Identify the blood parasite species.
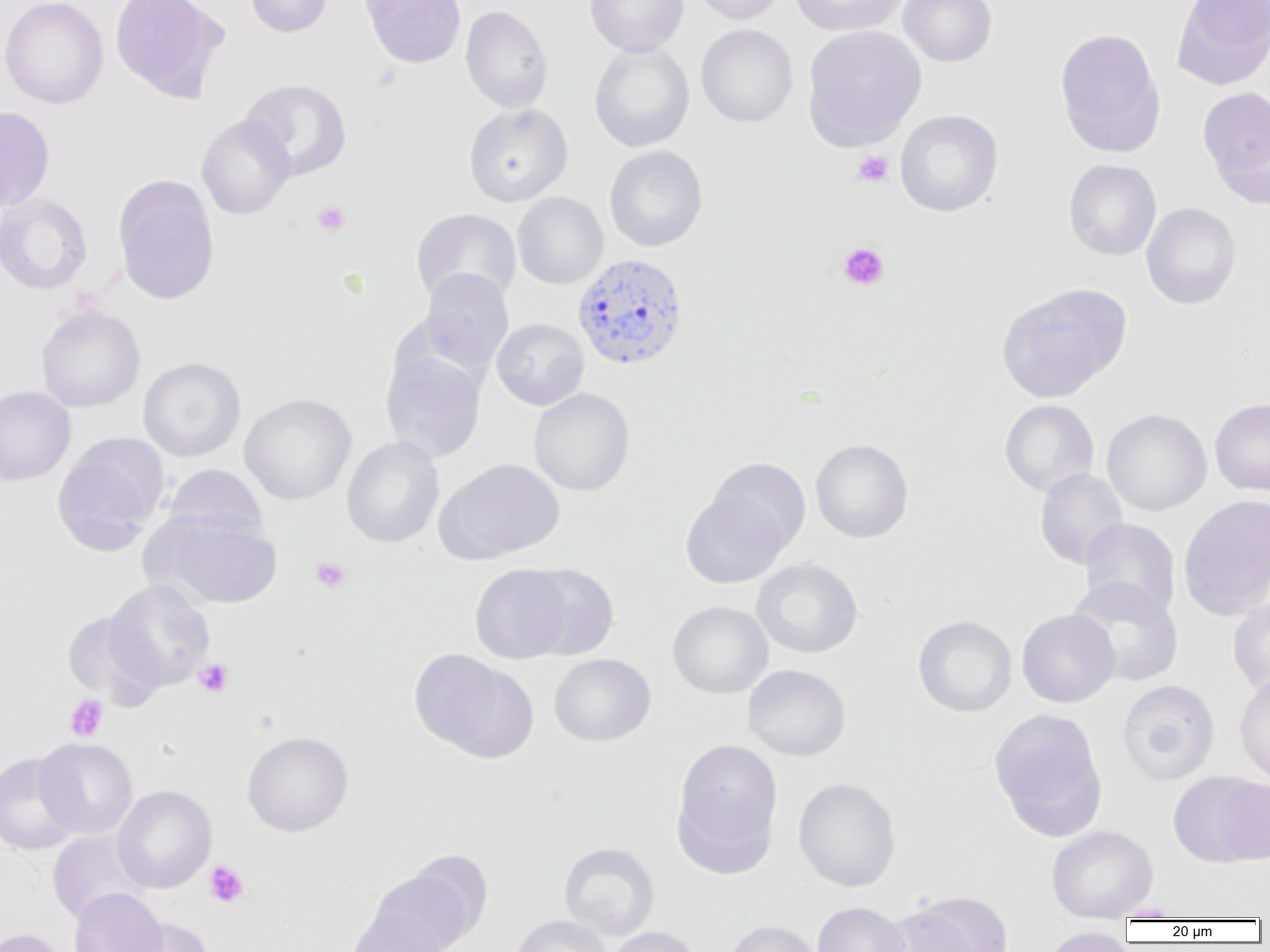

Plasmodium vivax.

uninfected red blood cell locations = approximate bounding boxes as (x1, y1, x2, y2) in pixels: (0, 0, 109, 108), (109, 0, 227, 101), (244, 0, 333, 37), (360, 0, 466, 68), (584, 0, 689, 57), (692, 0, 788, 25), (789, 0, 907, 36), (898, 0, 997, 67), (1173, 0, 1270, 90), (460, 4, 553, 113), (696, 24, 798, 127), (802, 25, 927, 150), (1055, 28, 1165, 158), (589, 42, 694, 151), (240, 78, 352, 181), (1198, 87, 1269, 202), (464, 103, 572, 206), (0, 106, 55, 212), (895, 109, 1003, 216), (196, 114, 296, 220), (605, 145, 707, 252), (1063, 159, 1161, 261), (113, 175, 220, 305), (512, 192, 608, 289), (0, 193, 92, 294), (1141, 202, 1241, 309), (411, 208, 521, 307), (417, 268, 513, 376), (996, 282, 1129, 403), (36, 305, 145, 412), (491, 318, 589, 410), (381, 351, 486, 462), (138, 356, 246, 462), (0, 386, 76, 485), (529, 387, 634, 495), (239, 393, 357, 505), (1210, 398, 1270, 496), (999, 399, 1099, 497), (1102, 408, 1212, 516), (52, 434, 168, 554), (341, 436, 445, 548), (811, 439, 913, 543), (441, 458, 565, 562), (706, 458, 811, 551), (161, 464, 267, 544), (1035, 468, 1129, 570), (681, 486, 790, 589), (1179, 494, 1270, 619), (157, 515, 282, 609), (1080, 517, 1180, 619), (751, 559, 862, 658), (470, 564, 572, 663), (521, 564, 619, 660), (1066, 576, 1184, 686), (103, 580, 215, 691), (1228, 597, 1270, 698), (667, 601, 773, 698), (61, 609, 163, 709), (1016, 609, 1120, 708), (913, 615, 1017, 717), (409, 648, 524, 757), (549, 653, 655, 746), (743, 664, 851, 761), (1234, 672, 1270, 784), (1117, 679, 1220, 784), (988, 708, 1108, 840), (242, 731, 353, 837), (35, 738, 137, 839), (671, 738, 783, 869), (0, 752, 83, 855), (1170, 772, 1269, 867), (793, 777, 901, 892), (112, 785, 216, 893), (1047, 825, 1158, 920), (47, 830, 150, 924), (559, 842, 659, 940), (366, 869, 471, 950), (69, 887, 168, 952), (891, 894, 1012, 952), (813, 901, 911, 952), (345, 910, 449, 952), (510, 914, 610, 952), (123, 918, 215, 952), (723, 919, 824, 952), (607, 926, 703, 952), (1039, 927, 1137, 952), (0, 928, 69, 952)
preparation = thin blood film
Plasmodium vivax-infected red blood cell locations = approximate bounding boxes as (x1, y1, x2, y2) in pixels: (572, 253, 690, 371)
image size = 1270×952 pixels
platelet locations = approximate bounding boxes as (x1, y1, x2, y2) in pixels: (852, 150, 893, 187), (313, 202, 350, 236), (837, 243, 890, 290), (310, 557, 351, 593), (194, 659, 233, 696), (65, 694, 109, 741), (205, 860, 248, 908)
field of view = single
modality = light microscopy
magnification = 1000x